Classify this cell by malaria status.
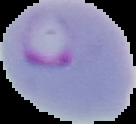

It is parasitized.

The area outside the segmented cell region is set to black. Image is 136×124 pixels. From a thin blood film.